Report the malaria status of this cell.
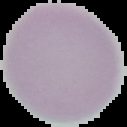

Uninfected.

Summary:
  - Image type: segmented cell region on a black background
  - Image size: 127×127 pixels
  - Preparation: thin blood film